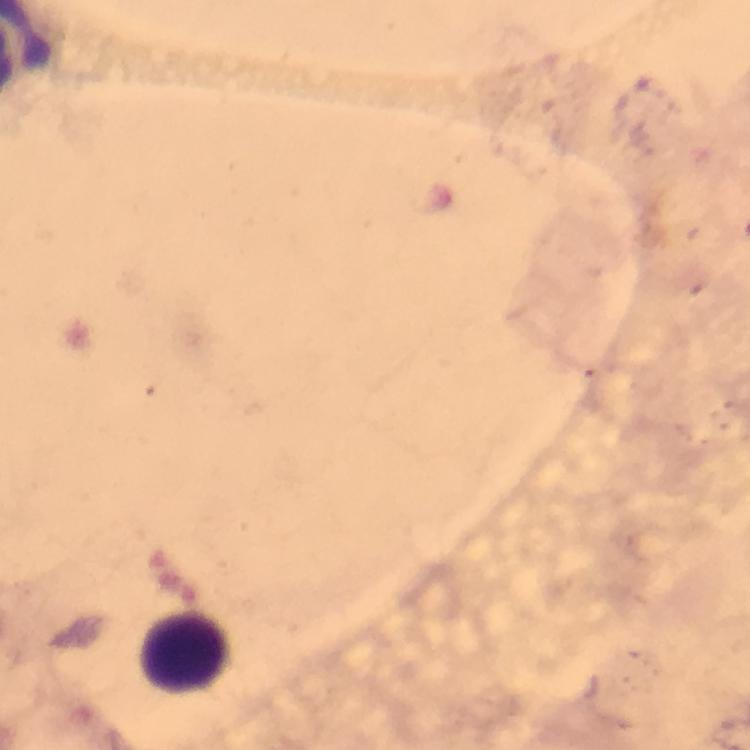

image size = 750×750 pixels
immersion oil = used
capture = smartphone mounted on the microscope
preparation = thick blood film
magnification = 100x
cropped from = a single field of view
context = from a malaria diagnostic workup
leukocyte locations = approximate centers as {x, y} in pixels: {189, 651}
Plasmodium parasites = none detected
stain = Giemsa